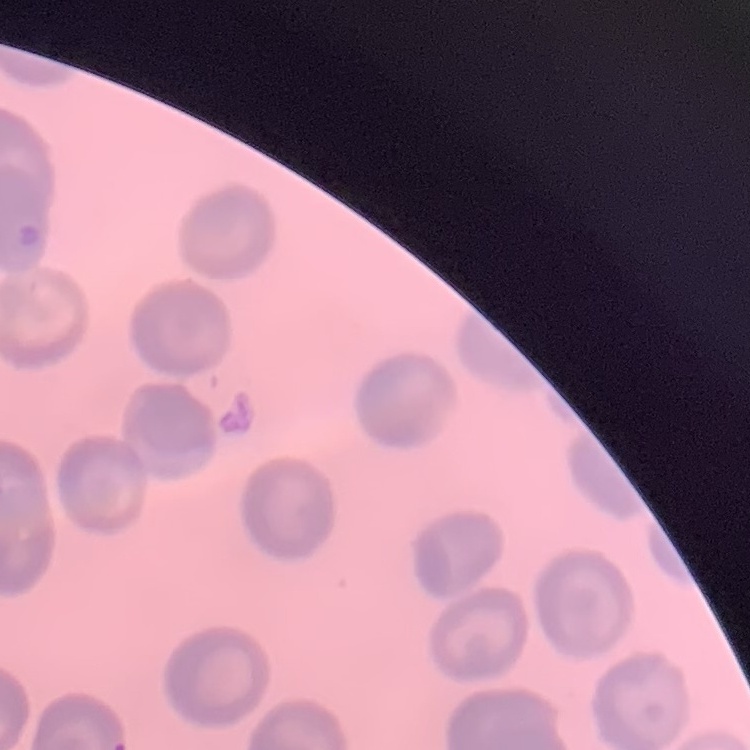 The red blood cells exhibit no rouleaux formation. Square crop of a larger photomicrograph. Thin blood smear. Stained with either Field's or Giemsa.